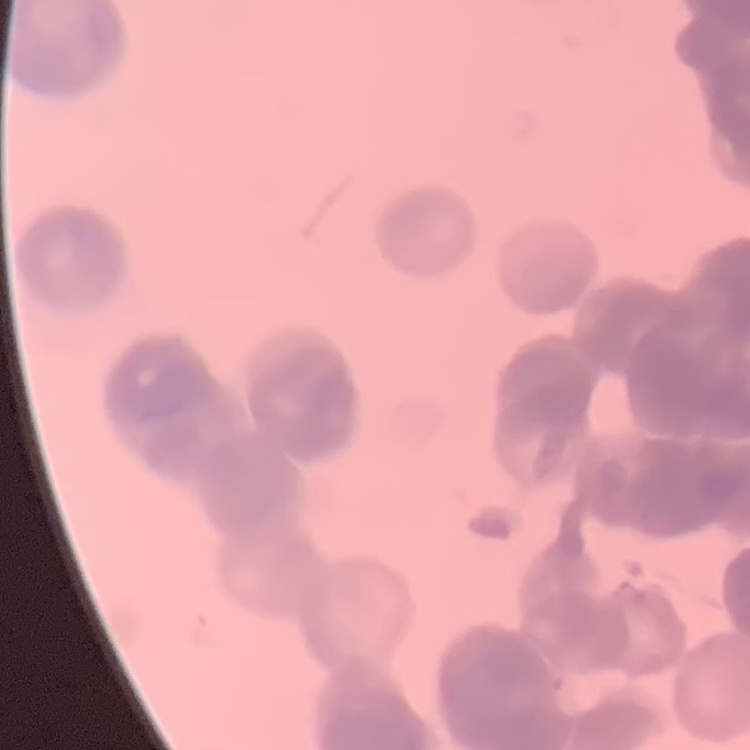
The erythrocytes show rouleaux formation. Thin blood smear. Field's or Giemsa stain. Square crop of a larger photomicrograph.